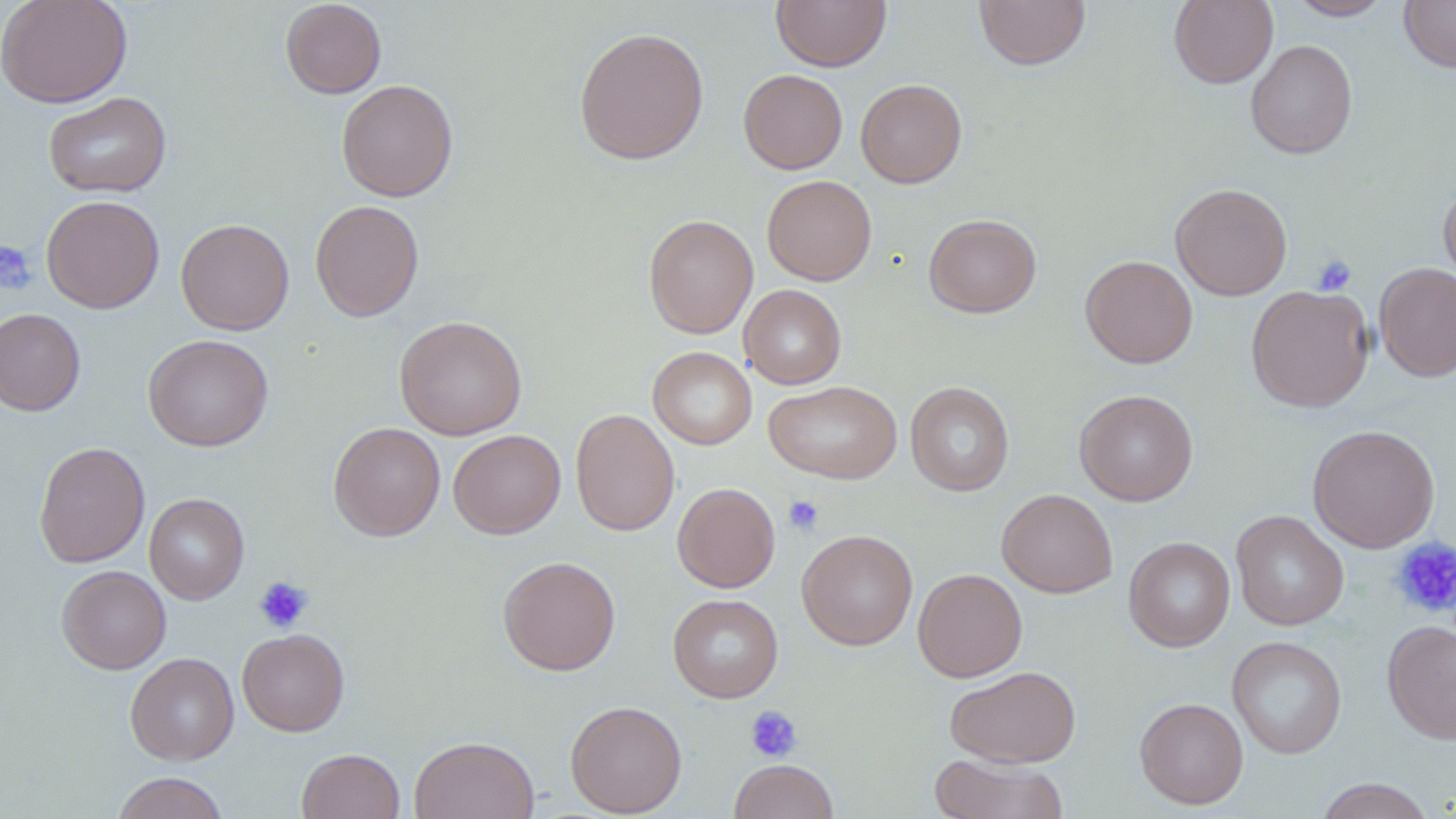 Approximate bounding boxes as named x1/y1/x2/y2 corners in pixels. Uninfected red blood cell locations: (x1=0, y1=0, x2=132, y2=108), (x1=280, y1=0, x2=387, y2=98), (x1=772, y1=0, x2=891, y2=71), (x1=974, y1=0, x2=1091, y2=70), (x1=1168, y1=0, x2=1278, y2=88), (x1=1288, y1=0, x2=1394, y2=21), (x1=1399, y1=0, x2=1456, y2=73), (x1=573, y1=26, x2=709, y2=165), (x1=1245, y1=39, x2=1358, y2=159), (x1=738, y1=69, x2=848, y2=174), (x1=855, y1=78, x2=967, y2=188), (x1=336, y1=79, x2=458, y2=201), (x1=43, y1=91, x2=172, y2=198), (x1=761, y1=175, x2=877, y2=286), (x1=1439, y1=181, x2=1456, y2=294), (x1=1170, y1=182, x2=1292, y2=301), (x1=41, y1=195, x2=165, y2=314), (x1=310, y1=199, x2=424, y2=321), (x1=643, y1=213, x2=758, y2=339), (x1=924, y1=213, x2=1042, y2=317), (x1=176, y1=218, x2=294, y2=335), (x1=1080, y1=254, x2=1198, y2=368), (x1=1373, y1=262, x2=1456, y2=383), (x1=1246, y1=284, x2=1374, y2=412), (x1=739, y1=285, x2=847, y2=389), (x1=0, y1=308, x2=85, y2=416), (x1=394, y1=315, x2=527, y2=440), (x1=143, y1=334, x2=273, y2=451), (x1=647, y1=346, x2=757, y2=450), (x1=764, y1=381, x2=902, y2=484), (x1=906, y1=381, x2=1014, y2=496), (x1=1074, y1=389, x2=1198, y2=506), (x1=570, y1=408, x2=680, y2=537), (x1=329, y1=422, x2=445, y2=541), (x1=1307, y1=424, x2=1440, y2=552), (x1=448, y1=429, x2=566, y2=539), (x1=34, y1=441, x2=150, y2=568), (x1=672, y1=482, x2=780, y2=592), (x1=997, y1=488, x2=1117, y2=598), (x1=145, y1=493, x2=249, y2=604), (x1=1230, y1=510, x2=1349, y2=631), (x1=797, y1=530, x2=917, y2=651), (x1=1123, y1=537, x2=1235, y2=652), (x1=497, y1=555, x2=621, y2=676), (x1=56, y1=565, x2=171, y2=674), (x1=913, y1=568, x2=1027, y2=682), (x1=668, y1=594, x2=783, y2=702), (x1=1381, y1=619, x2=1456, y2=743), (x1=237, y1=628, x2=349, y2=736), (x1=1227, y1=635, x2=1347, y2=759), (x1=125, y1=652, x2=239, y2=765), (x1=945, y1=665, x2=1081, y2=768), (x1=1135, y1=697, x2=1248, y2=809), (x1=565, y1=699, x2=687, y2=817), (x1=409, y1=735, x2=540, y2=819), (x1=297, y1=748, x2=405, y2=819), (x1=930, y1=753, x2=1069, y2=818), (x1=728, y1=759, x2=839, y2=819), (x1=111, y1=772, x2=229, y2=819), (x1=1314, y1=777, x2=1437, y2=819). Platelet locations: (x1=0, y1=240, x2=37, y2=295), (x1=1312, y1=253, x2=1357, y2=296), (x1=783, y1=494, x2=825, y2=535), (x1=1390, y1=536, x2=1456, y2=620), (x1=253, y1=576, x2=313, y2=633), (x1=745, y1=705, x2=802, y2=762). Slide-level diagnosis: no evidence of blood parasites. May-Grünwald-Giemsa stain. Single field of view. Optical microscopy. Captured at 1000x magnification. Image is 1456×819 pixels. Thin blood film.